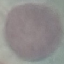 Result: negative for malaria parasites. Automatically extracted cell patch, resized to 64 × 64 pixels. Thin smear of blood. Acquired by smartphone through the microscope eyepiece. Giemsa stain.